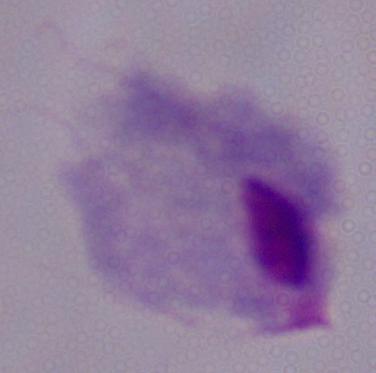 Photomicrograph. A trichomonad is seen. Captured at 1000x magnification.